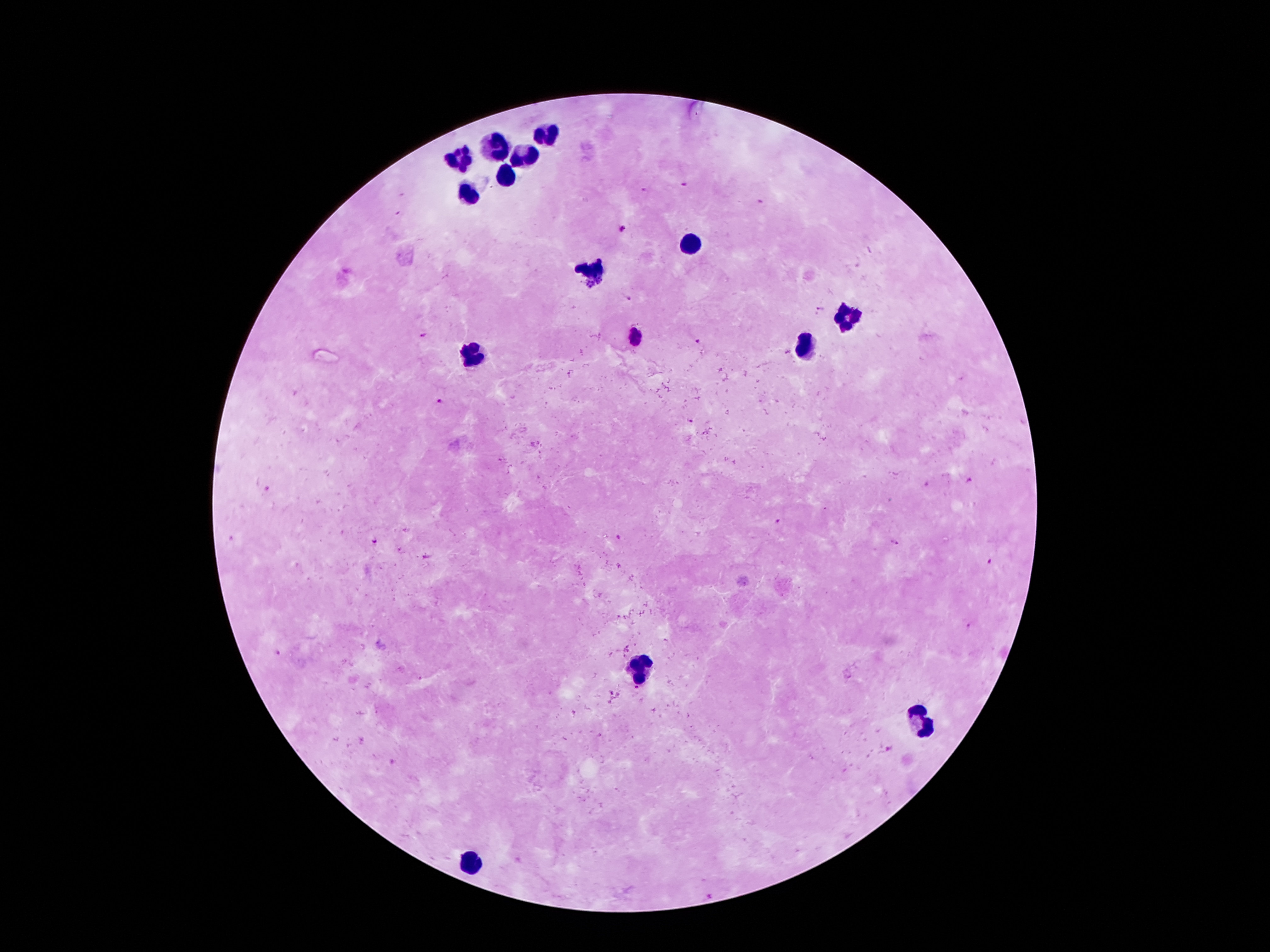
Approximate centers as (x, y) in pixels. Plasmodium parasite locations: (683, 185), (645, 190), (758, 200), (622, 230), (629, 299), (820, 308), (421, 337), (634, 340), (696, 341), (442, 401), (969, 481), (778, 522), (618, 538), (373, 540), (894, 541), (427, 558), (989, 561), (969, 626), (279, 653), (637, 688), (709, 895). Leukocyte locations: (549, 135), (494, 148), (465, 158), (528, 158), (507, 173), (465, 198), (692, 241), (591, 274), (847, 318), (805, 347), (475, 355), (643, 669), (923, 724), (471, 865). One field from this slide. Photographed through the microscope eyepiece with a smartphone camera. Image is 1270×952 pixels. 100x magnification. Patient malaria status: positive for Plasmodium falciparum. Thick blood smear. Giemsa-stained preparation.